Identify the blood parasite species.
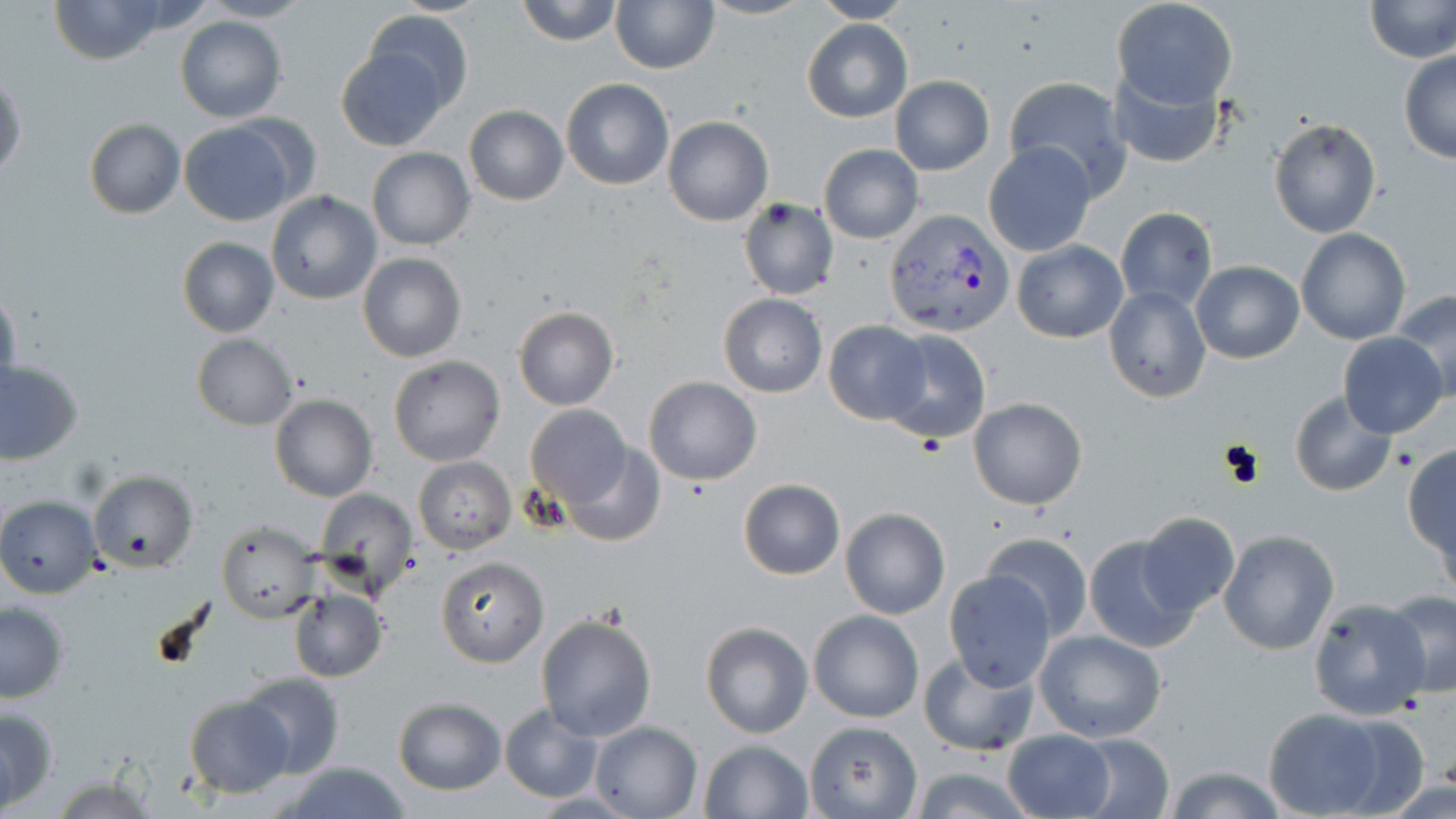
Plasmodium vivax.

Approximate bounding boxes as named x1/y1/x2/y2 corners in pixels. Plasmodium vivax-infected red blood cell locations: (x1=885, y1=209, x2=1012, y2=336). Uninfected red blood cell locations: (x1=45, y1=0, x2=173, y2=66), (x1=513, y1=0, x2=623, y2=46), (x1=699, y1=0, x2=813, y2=22), (x1=808, y1=0, x2=914, y2=24), (x1=1367, y1=0, x2=1456, y2=63), (x1=199, y1=1, x2=314, y2=23), (x1=612, y1=1, x2=719, y2=74), (x1=1112, y1=1, x2=1236, y2=114), (x1=358, y1=6, x2=472, y2=119), (x1=175, y1=15, x2=287, y2=122), (x1=802, y1=18, x2=912, y2=123), (x1=336, y1=47, x2=449, y2=151), (x1=1399, y1=50, x2=1456, y2=164), (x1=1113, y1=69, x2=1225, y2=167), (x1=1, y1=73, x2=25, y2=181), (x1=890, y1=75, x2=994, y2=175), (x1=1003, y1=76, x2=1129, y2=196), (x1=561, y1=78, x2=674, y2=190), (x1=463, y1=105, x2=567, y2=206), (x1=663, y1=116, x2=773, y2=226), (x1=178, y1=117, x2=307, y2=226), (x1=1267, y1=117, x2=1383, y2=239), (x1=83, y1=118, x2=186, y2=219), (x1=983, y1=141, x2=1097, y2=257), (x1=818, y1=143, x2=923, y2=245), (x1=366, y1=147, x2=476, y2=251), (x1=264, y1=190, x2=383, y2=306), (x1=736, y1=196, x2=839, y2=301), (x1=1117, y1=207, x2=1217, y2=311), (x1=1296, y1=229, x2=1410, y2=345), (x1=177, y1=238, x2=280, y2=338), (x1=1012, y1=240, x2=1127, y2=343), (x1=356, y1=251, x2=468, y2=363), (x1=1192, y1=260, x2=1303, y2=364), (x1=0, y1=283, x2=22, y2=403), (x1=1104, y1=286, x2=1210, y2=402), (x1=1393, y1=288, x2=1456, y2=404), (x1=719, y1=293, x2=827, y2=397), (x1=513, y1=307, x2=618, y2=411), (x1=824, y1=320, x2=931, y2=423), (x1=881, y1=330, x2=992, y2=448), (x1=1338, y1=332, x2=1448, y2=439), (x1=191, y1=333, x2=298, y2=429), (x1=388, y1=356, x2=505, y2=466), (x1=1, y1=360, x2=83, y2=464), (x1=644, y1=377, x2=761, y2=485), (x1=1289, y1=391, x2=1397, y2=497), (x1=269, y1=394, x2=377, y2=503), (x1=968, y1=396, x2=1088, y2=510), (x1=524, y1=405, x2=634, y2=506), (x1=557, y1=444, x2=664, y2=548), (x1=1403, y1=444, x2=1455, y2=566), (x1=413, y1=458, x2=515, y2=554), (x1=88, y1=469, x2=200, y2=573), (x1=739, y1=479, x2=844, y2=579), (x1=314, y1=489, x2=418, y2=599), (x1=0, y1=496, x2=100, y2=598), (x1=840, y1=507, x2=950, y2=619), (x1=1135, y1=513, x2=1239, y2=618), (x1=217, y1=519, x2=321, y2=624), (x1=1218, y1=530, x2=1340, y2=655), (x1=1084, y1=531, x2=1202, y2=653), (x1=982, y1=532, x2=1092, y2=641), (x1=436, y1=554, x2=548, y2=667), (x1=945, y1=571, x2=1058, y2=691), (x1=289, y1=588, x2=387, y2=682), (x1=1382, y1=589, x2=1456, y2=700), (x1=1307, y1=597, x2=1434, y2=721), (x1=0, y1=601, x2=71, y2=702), (x1=808, y1=610, x2=924, y2=723), (x1=534, y1=613, x2=657, y2=740), (x1=701, y1=621, x2=813, y2=738), (x1=1034, y1=630, x2=1168, y2=744), (x1=918, y1=650, x2=1039, y2=757), (x1=239, y1=672, x2=345, y2=778), (x1=184, y1=695, x2=294, y2=797), (x1=393, y1=697, x2=506, y2=795), (x1=1, y1=704, x2=58, y2=812), (x1=499, y1=704, x2=602, y2=803), (x1=1258, y1=707, x2=1405, y2=818), (x1=590, y1=721, x2=701, y2=818), (x1=804, y1=721, x2=922, y2=817), (x1=1000, y1=729, x2=1116, y2=819), (x1=1072, y1=734, x2=1175, y2=818), (x1=699, y1=740, x2=812, y2=818), (x1=278, y1=763, x2=411, y2=817), (x1=904, y1=763, x2=1038, y2=819), (x1=1158, y1=764, x2=1290, y2=819). Optical microscopy. Thin blood smear. Image is 1456×819 pixels. One field of a larger specimen. May-Grünwald-Giemsa stain. Captured at 1000x magnification.